Locate every Plasmodium parasite.
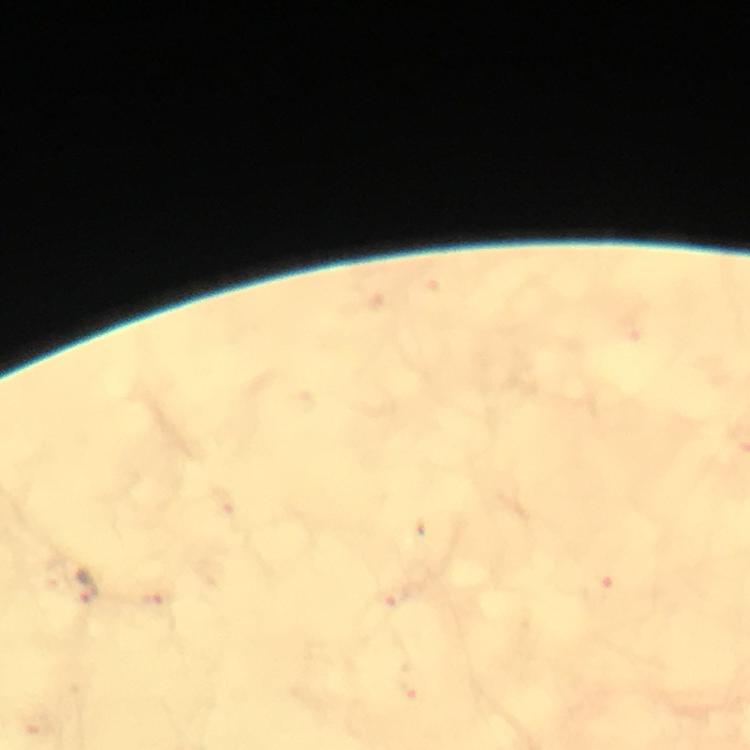
Approximate centers as [x, y] in pixels.
Plasmodium parasites: [86, 585].

immersion oil = applied
magnification = 100x
context = from a diagnostic examination for malaria
capture = smartphone photograph through a microscope
cropped from = a single field of view
preparation = thick blood smear
image size = 750×750 pixels
stain = Giemsa